Outline each blood parasite and name the species.
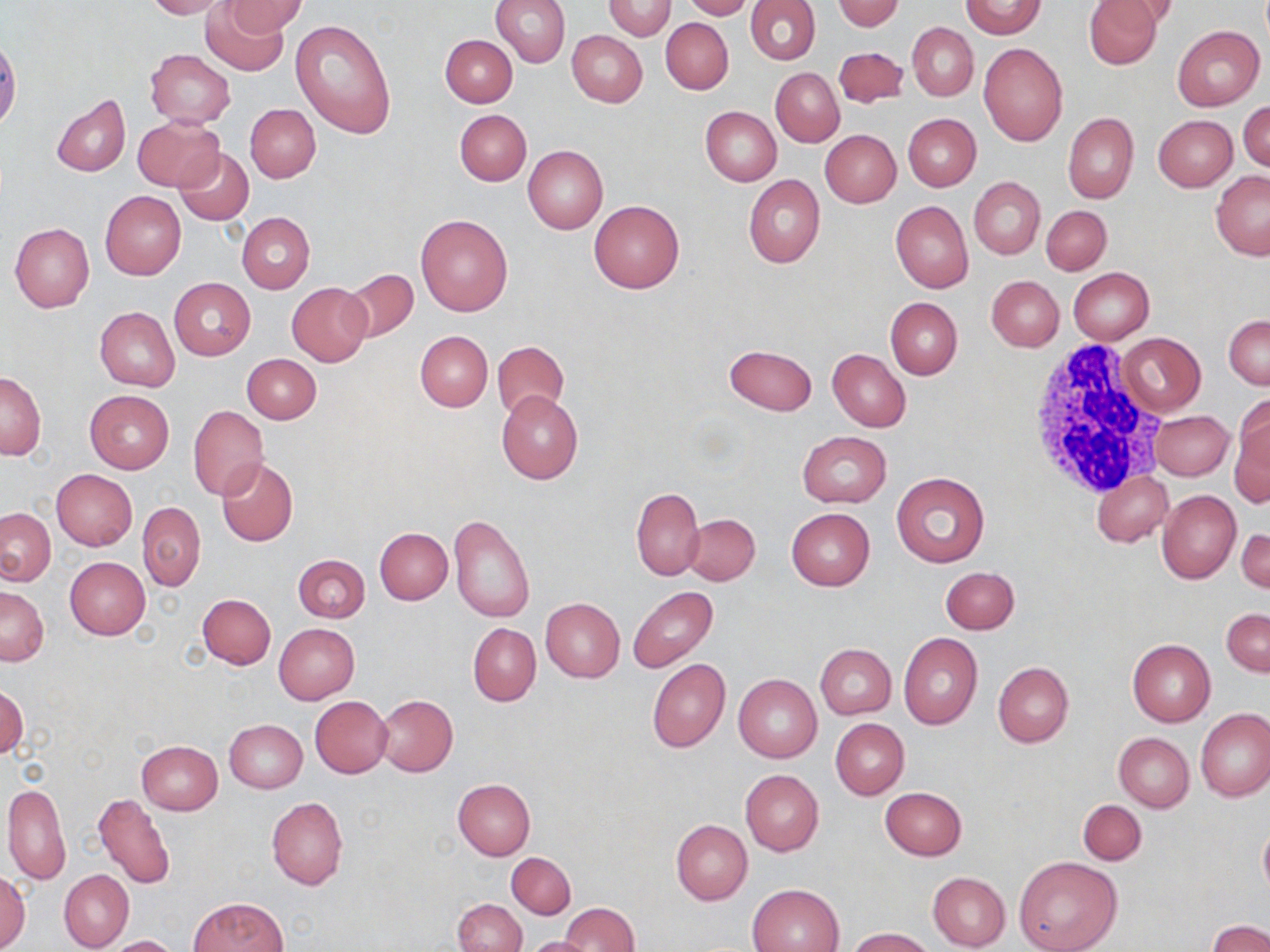

No blood parasites observed.

Summary:
  - Coordinate format: approximate bounding boxes as named x1/y1/x2/y2 corners in pixels
  - Uninfected red blood cell locations: (x1=143, y1=0, x2=230, y2=19), (x1=201, y1=0, x2=292, y2=75), (x1=224, y1=0, x2=308, y2=37), (x1=490, y1=0, x2=571, y2=67), (x1=603, y1=0, x2=675, y2=40), (x1=681, y1=0, x2=756, y2=20), (x1=745, y1=0, x2=820, y2=66), (x1=835, y1=0, x2=903, y2=31), (x1=1082, y1=0, x2=1165, y2=69), (x1=960, y1=1, x2=1046, y2=38), (x1=1098, y1=1, x2=1181, y2=29), (x1=290, y1=18, x2=397, y2=136), (x1=661, y1=18, x2=733, y2=94), (x1=907, y1=22, x2=979, y2=101), (x1=1172, y1=24, x2=1265, y2=111), (x1=567, y1=30, x2=647, y2=107), (x1=440, y1=34, x2=518, y2=107), (x1=978, y1=43, x2=1068, y2=148), (x1=833, y1=47, x2=907, y2=107), (x1=146, y1=50, x2=236, y2=127), (x1=770, y1=68, x2=844, y2=147), (x1=52, y1=94, x2=131, y2=177), (x1=1239, y1=100, x2=1269, y2=173), (x1=245, y1=104, x2=320, y2=183), (x1=701, y1=107, x2=781, y2=186), (x1=455, y1=109, x2=531, y2=186), (x1=1063, y1=112, x2=1138, y2=204), (x1=902, y1=113, x2=981, y2=191), (x1=1154, y1=115, x2=1237, y2=191), (x1=133, y1=116, x2=224, y2=192), (x1=820, y1=130, x2=900, y2=207), (x1=523, y1=145, x2=608, y2=234), (x1=174, y1=147, x2=254, y2=226), (x1=1211, y1=169, x2=1270, y2=260), (x1=743, y1=175, x2=825, y2=268), (x1=969, y1=177, x2=1045, y2=259), (x1=100, y1=191, x2=186, y2=279), (x1=891, y1=200, x2=973, y2=293), (x1=589, y1=201, x2=685, y2=293), (x1=1043, y1=205, x2=1111, y2=276), (x1=237, y1=213, x2=315, y2=293), (x1=416, y1=213, x2=513, y2=317), (x1=10, y1=222, x2=94, y2=312), (x1=1068, y1=268, x2=1155, y2=344), (x1=344, y1=269, x2=418, y2=343), (x1=986, y1=276, x2=1063, y2=351), (x1=169, y1=277, x2=255, y2=360), (x1=288, y1=282, x2=372, y2=366), (x1=886, y1=297, x2=962, y2=379), (x1=96, y1=306, x2=180, y2=391), (x1=1224, y1=314, x2=1269, y2=388), (x1=415, y1=330, x2=493, y2=411), (x1=1117, y1=332, x2=1205, y2=417), (x1=492, y1=340, x2=568, y2=420), (x1=724, y1=343, x2=817, y2=416), (x1=827, y1=349, x2=910, y2=432), (x1=244, y1=353, x2=321, y2=423), (x1=1, y1=372, x2=45, y2=461), (x1=84, y1=390, x2=173, y2=474), (x1=496, y1=391, x2=583, y2=484), (x1=1229, y1=402, x2=1270, y2=506), (x1=188, y1=405, x2=268, y2=501), (x1=1152, y1=410, x2=1233, y2=480), (x1=797, y1=431, x2=891, y2=508), (x1=216, y1=458, x2=298, y2=547), (x1=51, y1=469, x2=137, y2=551), (x1=892, y1=471, x2=989, y2=567), (x1=1091, y1=471, x2=1172, y2=547), (x1=631, y1=488, x2=705, y2=580), (x1=1156, y1=489, x2=1240, y2=584), (x1=138, y1=501, x2=206, y2=589), (x1=1, y1=508, x2=55, y2=585), (x1=786, y1=508, x2=875, y2=591), (x1=684, y1=513, x2=760, y2=586), (x1=448, y1=514, x2=534, y2=622), (x1=1236, y1=527, x2=1270, y2=593), (x1=375, y1=528, x2=453, y2=604), (x1=293, y1=554, x2=370, y2=623), (x1=65, y1=556, x2=150, y2=639), (x1=940, y1=566, x2=1019, y2=633), (x1=0, y1=586, x2=49, y2=666), (x1=627, y1=586, x2=718, y2=672), (x1=197, y1=593, x2=276, y2=668), (x1=540, y1=597, x2=625, y2=682), (x1=1222, y1=608, x2=1269, y2=676), (x1=274, y1=623, x2=359, y2=703), (x1=468, y1=624, x2=540, y2=705), (x1=898, y1=632, x2=983, y2=730), (x1=1127, y1=638, x2=1215, y2=726), (x1=816, y1=643, x2=896, y2=719), (x1=647, y1=658, x2=730, y2=752), (x1=992, y1=661, x2=1075, y2=747), (x1=733, y1=674, x2=822, y2=762), (x1=1, y1=685, x2=28, y2=761), (x1=375, y1=694, x2=458, y2=775), (x1=310, y1=696, x2=392, y2=777), (x1=1196, y1=708, x2=1269, y2=802), (x1=830, y1=719, x2=908, y2=799), (x1=225, y1=720, x2=306, y2=792), (x1=1113, y1=733, x2=1194, y2=812), (x1=135, y1=740, x2=222, y2=815), (x1=740, y1=769, x2=823, y2=857), (x1=454, y1=779, x2=536, y2=859), (x1=3, y1=783, x2=71, y2=885), (x1=880, y1=787, x2=966, y2=859), (x1=93, y1=792, x2=176, y2=890), (x1=266, y1=796, x2=348, y2=890), (x1=1077, y1=799, x2=1146, y2=865), (x1=670, y1=819, x2=752, y2=904), (x1=1258, y1=819, x2=1270, y2=900), (x1=506, y1=852, x2=575, y2=918), (x1=1012, y1=855, x2=1123, y2=952), (x1=1, y1=870, x2=31, y2=949), (x1=60, y1=870, x2=134, y2=951), (x1=928, y1=871, x2=1011, y2=950), (x1=748, y1=883, x2=844, y2=951), (x1=189, y1=896, x2=286, y2=952), (x1=453, y1=899, x2=525, y2=952), (x1=560, y1=902, x2=638, y2=952), (x1=1207, y1=920, x2=1270, y2=952), (x1=849, y1=927, x2=934, y2=952), (x1=106, y1=935, x2=178, y2=951), (x1=523, y1=935, x2=597, y2=952)
  - White blood cell locations: (x1=1025, y1=341, x2=1165, y2=496)
  - Slide-level diagnosis: no evidence of blood parasites
  - Modality: optical microscopy
  - Field of view: single
  - Stain: May-Grünwald-Giemsa
  - Preparation: thin blood smear
  - Image size: 1270×952 pixels
  - Magnification: 1000x